Describe the morphology of the erythrocytes.
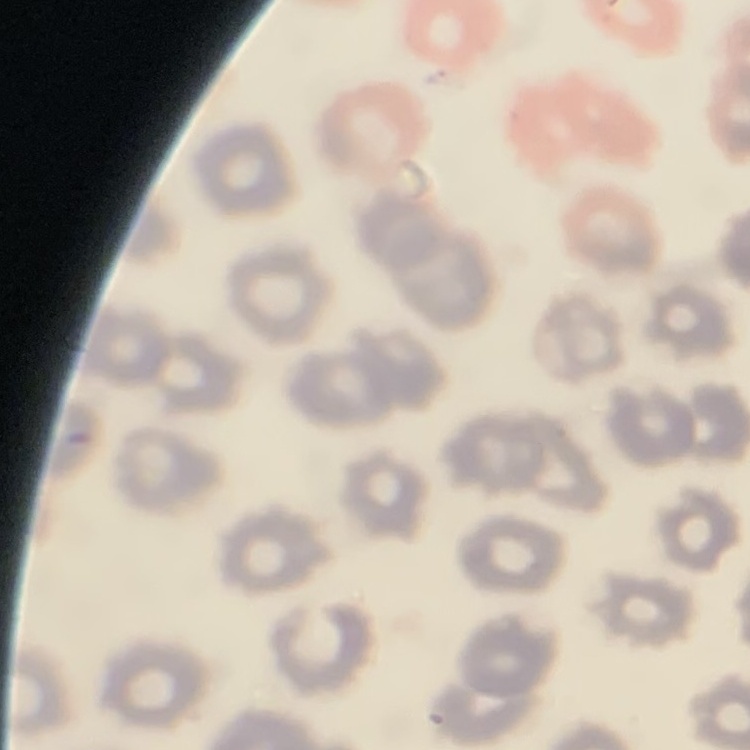

They show no rouleaux formation.

Summary:
  - Image type: square crop of a larger photomicrograph
  - Preparation: thin peripheral smear
  - Stain: Field's or Giemsa